Report the malaria status of this cell.
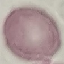
Uninfected.

Summary:
  - Stain: Giemsa
  - Capture: smartphone camera at the microscope eyepiece
  - Preparation: thin smear
  - Image type: automatically extracted cell patch, resized to 64 × 64 pixels